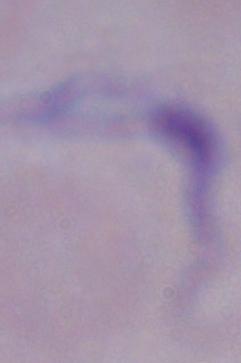

1000x magnification. Micrograph. A trypanosome is seen.